Comment on the morphology of the erythrocytes.
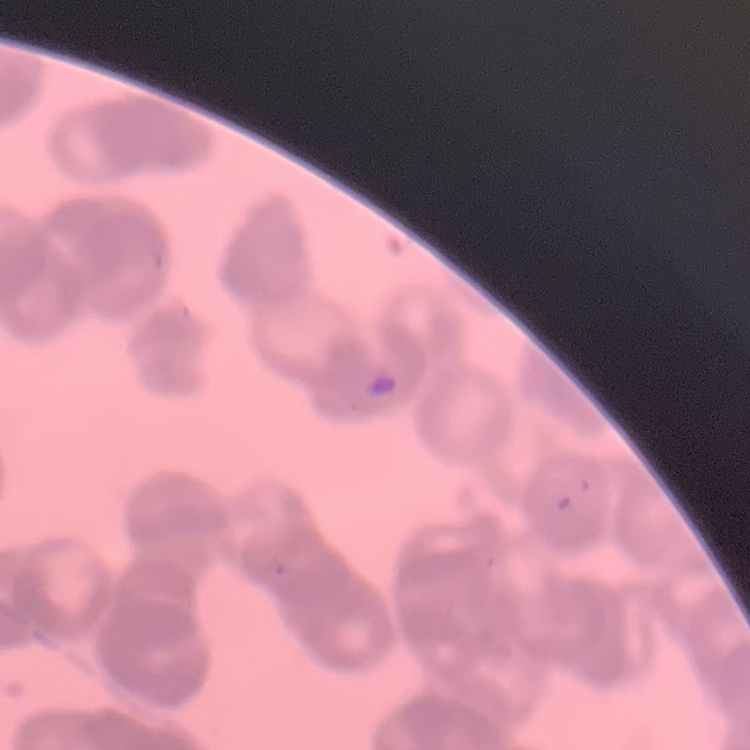

Rouleaux formation.

Summary:
  - Stain: Field's or Giemsa
  - Image type: one tile cut from a larger photomicrograph
  - Preparation: thin peripheral smear